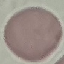

result = no malaria parasites seen
image type = cell patch, automatically extracted from a larger field of view and resized to 64 × 64 pixels
stain = Giemsa
preparation = thin blood smear
capture = smartphone through the microscope eyepiece